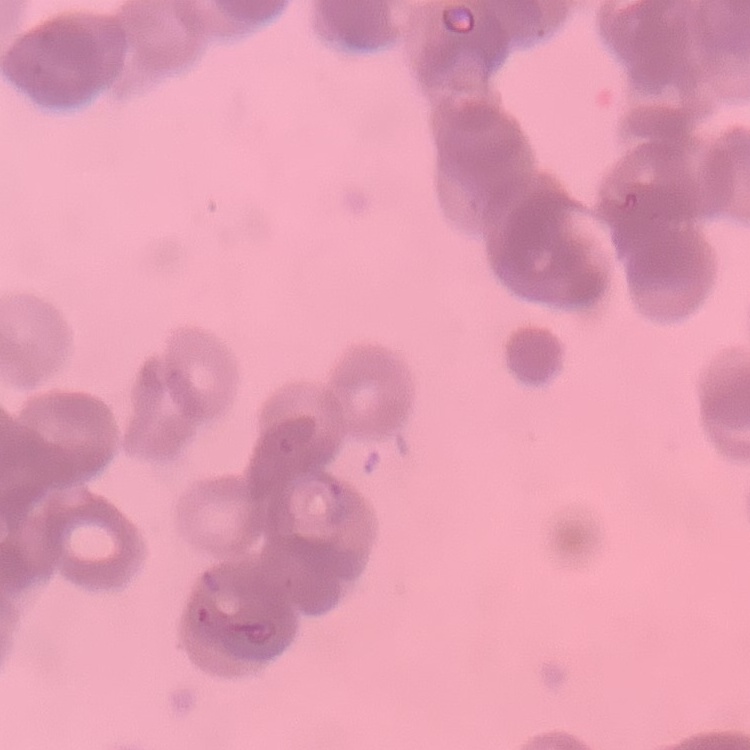
erythrocyte morphology = rouleaux formation
image type = square crop of a larger photomicrograph
stain = Field's or Giemsa
preparation = thin blood film